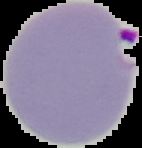

image type = segmented cell region with the area outside set to black
preparation = thin blood film
malaria status = parasitized
image size = 142×148 pixels